Name the parasite shown.
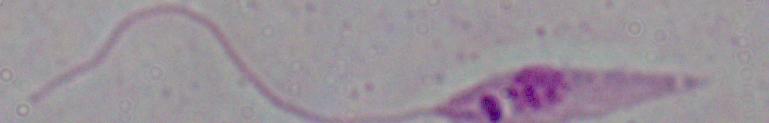

This is Leishmania.

magnification = 1000x
modality = photomicrograph